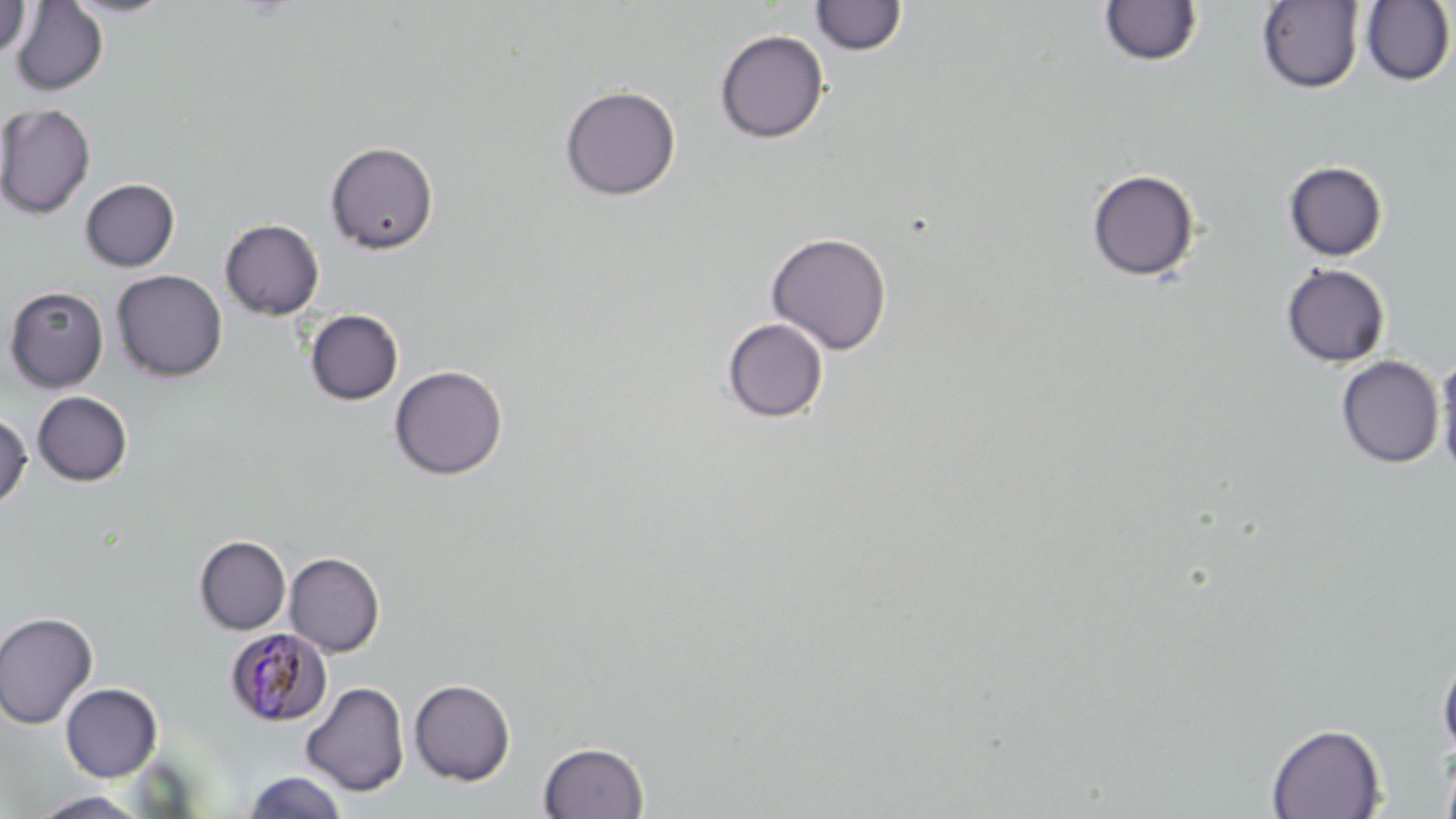

slide-level diagnosis = Plasmodium malariae
uninfected red blood cell locations = approximate bounding boxes as (x1,y1)-(x2,y2) corner pairs in pixels: (0,0)-(30,59), (60,0)-(180,19), (10,1)-(109,96), (810,1)-(908,56), (1098,1)-(1204,67), (1256,1)-(1365,93), (1360,1)-(1455,86), (713,29)-(829,143), (559,84)-(681,201), (0,103)-(96,219), (326,140)-(439,254), (1283,161)-(1388,261), (1086,168)-(1200,282), (80,178)-(180,271), (220,218)-(324,320), (766,231)-(892,355), (1281,263)-(1391,367), (112,270)-(227,382), (4,286)-(109,393), (304,309)-(404,406), (721,317)-(830,423), (1435,349)-(1456,485), (1335,355)-(1445,468), (389,365)-(508,480), (32,391)-(133,486), (0,410)-(32,510), (194,536)-(291,634), (284,552)-(385,656), (0,611)-(99,729), (1437,646)-(1456,763), (409,679)-(516,786), (301,681)-(410,796), (60,682)-(163,782), (1266,723)-(1386,818), (538,740)-(649,819), (1439,744)-(1456,819), (243,770)-(349,818), (26,791)-(153,818)
image size = 1456×819 pixels
stain = May-Grünwald-Giemsa
Plasmodium malariae-infected red blood cell locations = approximate bounding boxes as (x1,y1)-(x2,y2) corner pairs in pixels: (224,627)-(332,727)
field of view = single
modality = optical microscopy
preparation = thin blood smear
magnification = 1000x